Locate every Plasmodium parasite.
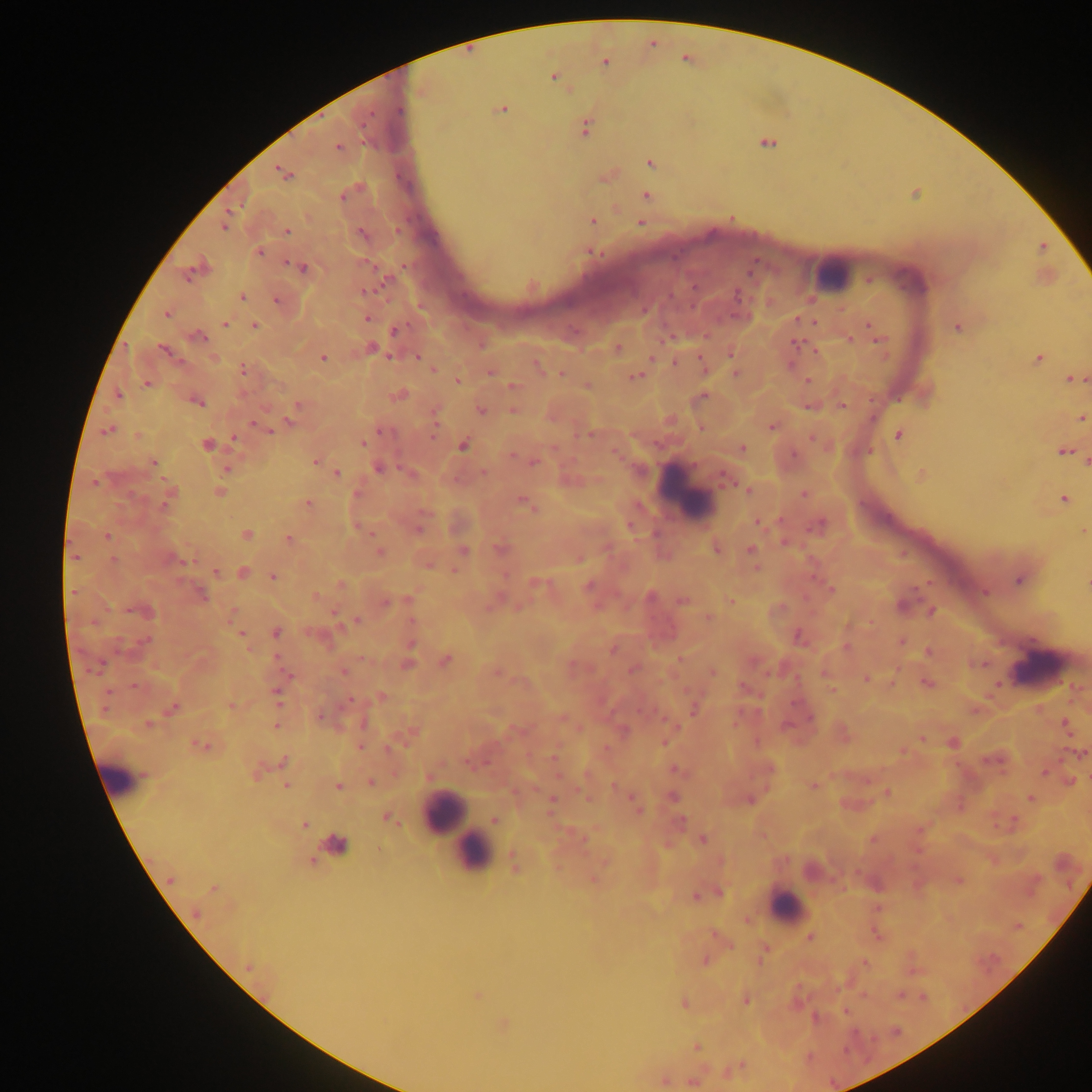
Approximate centers as x y in pixels.
Plasmodium parasites: 605 62; 553 76; 502 109; 399 110; 586 127; 767 142; 338 148; 651 164; 283 173; 647 196; 343 197; 592 221; 641 224; 225 225; 287 232; 362 234; 1043 247; 260 252; 594 252; 302 267; 189 277; 869 279; 385 282; 364 291; 737 296; 242 297; 277 300; 166 314; 367 319; 799 320; 815 323; 224 324; 869 325; 254 326; 957 328; 395 331; 198 337; 849 339; 880 339; 796 344; 372 348; 618 348; 165 351; 731 354; 323 357; 390 357; 417 357; 1039 358; 675 362; 537 364; 244 369; 433 369; 491 372; 560 374; 736 374; 637 376; 1072 380; 808 381; 458 382; 147 383; 512 386; 399 395; 118 396; 704 396; 198 402; 298 404; 843 406; 481 410; 513 411; 1082 418; 290 423; 257 425; 772 427; 701 428; 265 429; 108 430; 433 431; 383 432; 589 435; 899 435; 234 438; 812 438; 363 443; 207 445; 463 445; 742 449; 1064 451; 793 456; 153 462; 316 462; 534 462; 378 468; 227 470; 336 472; 483 472; 923 475; 726 477; 95 483; 748 490; 219 492; 804 493; 355 494; 1064 499; 308 504; 525 504; 166 505; 757 521; 820 524; 419 529; 1083 531; 246 534; 107 536; 289 539; 785 542; 500 548; 716 549; 751 551; 380 552; 464 552; 75 557; 172 559; 114 560; 429 566; 216 572; 243 573; 272 576; 1018 580; 537 582; 1087 585; 588 586; 831 589; 74 592; 985 593; 201 594; 317 596; 650 598; 409 599; 682 601; 731 601; 386 602; 144 611; 932 612; 709 618; 357 620; 412 621; 276 633; 242 636; 799 637; 144 641; 902 641; 411 645; 846 647; 613 650; 928 652; 445 660; 408 664; 98 667; 633 670; 343 672; 712 672; 866 678; 928 683; 832 690; 277 697; 380 697; 232 706; 174 708; 694 708; 320 716; 810 717; 149 723; 277 725; 787 725; 1065 725; 922 738; 665 742; 756 742; 200 745; 360 747; 389 748; 1080 754; 553 757; 283 761; 676 770; 1044 772; 1071 781; 371 782; 287 785; 338 785; 813 786; 887 792; 674 796; 1030 799; 551 801; 634 803; 638 810; 388 819; 494 820; 681 820; 304 825; 703 839; 584 841; 336 845; 312 861; 515 865; 170 879; 594 880; 959 880; 213 888; 720 894; 695 897; 197 913; 810 938; 864 962; 248 966; 477 996; 746 1000; 684 1003; 845 1011; 696 1047; 664 1080; 692 1082.

Leukocyte locations: 829 272; 688 490; 1038 664; 123 777; 444 812; 459 828; 473 852; 788 906. Thick blood film. One field of view. Mobile-phone photograph taken through the microscope. Sample from Ghana. Image is 1092×1092 pixels.